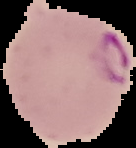
image type = segmented cell region on a black background
malaria status = parasitized
preparation = thin blood smear
image size = 136×148 pixels